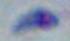
1000x magnification. Photomicrograph. Toxoplasma gondii is shown.